Outline each blood parasite and name the species.
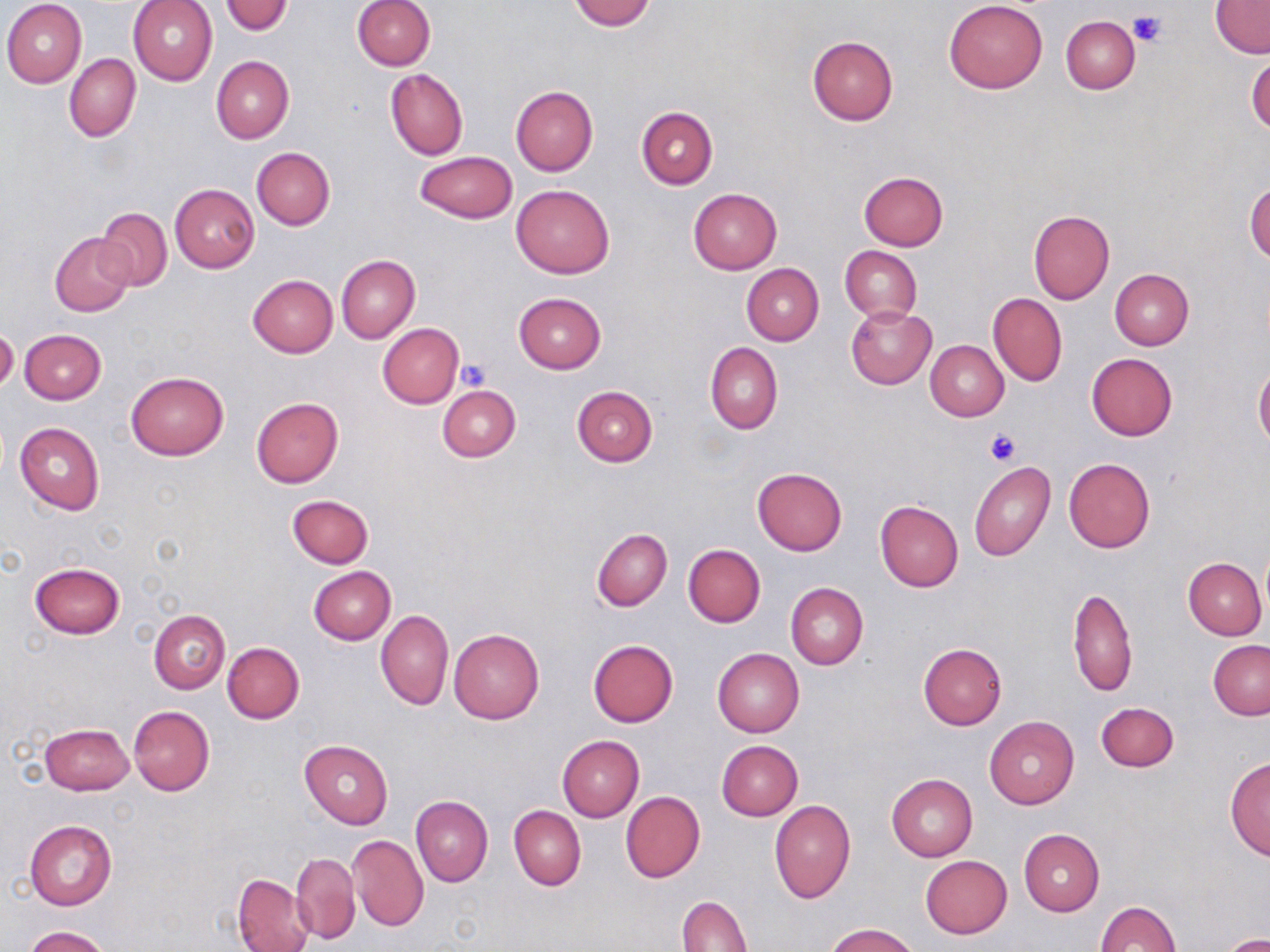

No blood parasites observed.

slide-level diagnosis = negative for blood parasites
image size = 1270×952 pixels
field of view = single
stain = May-Grünwald-Giemsa
platelet locations = approximate bounding boxes as (x1,y1)-(x2,y2) corner pairs in pixels: (1128,10)-(1165,48), (456,360)-(490,390), (984,428)-(1021,467)
uninfected red blood cell locations = approximate bounding boxes as (x1,y1)-(x2,y2) corner pairs in pixels: (1,0)-(86,87), (127,0)-(217,86), (221,0)-(292,36), (351,0)-(435,70), (568,0)-(655,30), (943,1)-(1048,94), (1211,1)-(1270,57), (1060,16)-(1140,94), (807,35)-(898,125), (64,53)-(140,142), (210,55)-(294,144), (1247,55)-(1270,134), (385,68)-(468,160), (511,85)-(598,175), (637,105)-(718,189), (251,147)-(335,230), (415,151)-(516,222), (859,172)-(948,251), (1246,180)-(1270,263), (511,183)-(615,279), (170,184)-(259,272), (688,188)-(781,275), (96,207)-(172,290), (1028,210)-(1114,305), (50,233)-(134,317), (838,245)-(921,323), (337,254)-(419,343), (741,264)-(823,346), (1109,268)-(1194,350), (247,274)-(338,358), (989,291)-(1067,387), (513,292)-(606,373), (847,306)-(936,387), (377,324)-(463,407), (1,327)-(21,394), (20,329)-(106,404), (926,340)-(1009,420), (705,341)-(782,434), (1086,352)-(1176,441), (1254,361)-(1270,450), (126,371)-(228,461), (571,385)-(658,467), (438,386)-(520,462), (251,398)-(343,487), (14,422)-(104,515), (1063,458)-(1156,553), (969,462)-(1055,562), (752,467)-(847,555), (286,495)-(373,569), (874,499)-(963,591), (591,528)-(672,610), (683,543)-(765,628), (1184,558)-(1267,639), (30,562)-(125,639), (309,566)-(394,645), (785,583)-(868,669), (1068,587)-(1137,697), (148,610)-(229,694), (377,610)-(453,710), (449,629)-(544,724), (589,639)-(677,727), (1209,639)-(1270,719), (222,642)-(304,724), (917,643)-(1007,730), (712,648)-(805,737), (1095,702)-(1179,772), (128,705)-(214,796), (985,716)-(1079,808), (40,723)-(134,795), (557,735)-(644,821), (299,740)-(392,828), (717,741)-(803,821), (1225,758)-(1270,860), (887,774)-(977,861), (621,791)-(705,883), (410,795)-(492,887), (770,800)-(856,903), (510,805)-(586,890), (24,818)-(117,911), (1018,828)-(1105,916), (349,834)-(428,931), (290,853)-(360,944), (920,855)-(1011,939), (231,873)-(314,952), (677,896)-(752,951), (1096,900)-(1180,951), (823,923)-(918,952), (23,926)-(110,952), (1219,934)-(1270,952)
preparation = thin blood smear
magnification = 1000x
modality = optical microscopy